Outline each blood parasite and name the species.
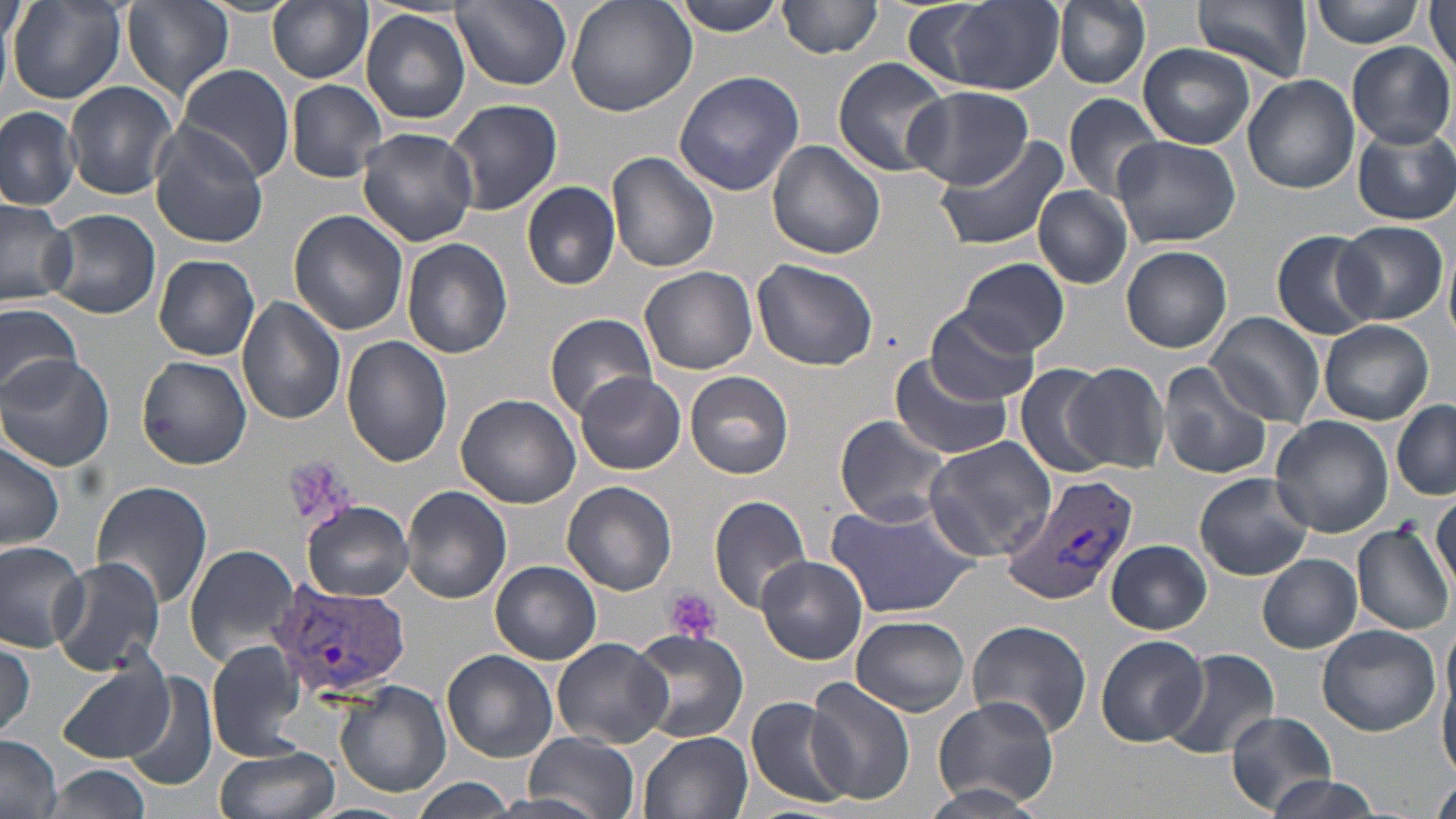
Approximate bounding boxes as (x1, y1, x2, y2) in pixels.
Plasmodium vivax-infected red blood cells: (999, 470, 1136, 608), (267, 579, 409, 702).
No Plasmodium falciparum, Plasmodium ovale, Plasmodium malariae, Babesia divergens, or Trypanosoma brucei observed.

Summary:
  - Platelet locations: (281, 456, 354, 531), (664, 589, 722, 643)
  - Uninfected red blood cell locations: (3, 0, 29, 51), (7, 0, 126, 105), (267, 0, 373, 84), (453, 0, 571, 90), (564, 0, 698, 117), (672, 0, 787, 36), (778, 0, 886, 59), (1055, 0, 1150, 89), (1193, 0, 1312, 83), (1311, 0, 1425, 47), (122, 1, 235, 100), (1428, 1, 1456, 82), (919, 2, 1066, 96), (1, 9, 14, 102), (360, 9, 471, 125), (1348, 40, 1453, 146), (1139, 43, 1255, 147), (833, 58, 952, 177), (177, 65, 295, 179), (673, 70, 806, 196), (1243, 72, 1359, 194), (285, 79, 386, 182), (66, 82, 178, 200), (905, 85, 1031, 189), (1063, 93, 1164, 202), (444, 96, 563, 215), (0, 106, 80, 209), (148, 124, 271, 247), (1353, 124, 1455, 225), (356, 127, 478, 246), (934, 133, 1070, 251), (1111, 136, 1240, 246), (767, 140, 886, 260), (606, 153, 719, 277), (522, 181, 620, 290), (1034, 186, 1134, 288), (0, 197, 76, 308), (43, 208, 161, 319), (290, 209, 409, 336), (1338, 222, 1446, 324), (1271, 230, 1382, 339), (401, 238, 513, 359), (1443, 242, 1456, 343), (1120, 246, 1233, 353), (153, 254, 261, 361), (751, 258, 878, 371), (955, 258, 1070, 357), (640, 266, 759, 376), (236, 296, 348, 426), (0, 300, 83, 401), (925, 305, 1041, 405), (1206, 311, 1325, 425), (545, 313, 658, 419), (1318, 319, 1435, 424), (341, 335, 452, 465), (1, 353, 114, 473), (886, 355, 1013, 461), (138, 356, 252, 468), (1156, 360, 1275, 479), (1013, 363, 1114, 479), (1065, 363, 1172, 473), (684, 371, 795, 479), (573, 372, 688, 476), (455, 395, 582, 508), (1391, 401, 1456, 501), (834, 414, 955, 527), (1269, 415, 1394, 538), (922, 436, 1060, 565), (0, 439, 64, 553), (1193, 471, 1313, 580), (90, 481, 214, 612), (563, 481, 677, 596), (400, 486, 513, 604), (1431, 489, 1456, 593), (707, 494, 811, 614), (824, 498, 981, 621), (301, 500, 414, 601), (1350, 523, 1454, 635), (1106, 539, 1211, 634), (0, 540, 90, 651), (184, 544, 300, 665), (1257, 554, 1361, 652), (48, 555, 166, 678), (756, 556, 868, 665), (491, 561, 602, 665), (1442, 616, 1455, 735), (850, 617, 973, 715), (967, 620, 1094, 737), (1316, 623, 1441, 736), (626, 628, 749, 744), (1096, 635, 1207, 746), (551, 637, 672, 749), (204, 638, 310, 760), (0, 640, 36, 742), (1162, 647, 1280, 758), (443, 650, 559, 763), (57, 658, 177, 763), (1440, 660, 1456, 782), (121, 672, 218, 793), (805, 678, 914, 806), (335, 681, 450, 801), (745, 695, 851, 807), (931, 697, 1060, 809), (1224, 709, 1336, 816), (640, 731, 753, 819), (522, 733, 642, 814), (0, 737, 64, 819), (215, 745, 341, 819), (44, 765, 150, 818), (1262, 774, 1381, 819), (1430, 776, 1456, 819), (411, 778, 516, 816), (914, 782, 1047, 819), (491, 794, 617, 819), (298, 802, 418, 819)
  - Slide-level diagnosis: Plasmodium vivax
  - Magnification: 1000x
  - Stain: May-Grünwald-Giemsa
  - Image size: 1456×819 pixels
  - Modality: optical microscopy
  - Field of view: one of a larger specimen
  - Preparation: thin blood film